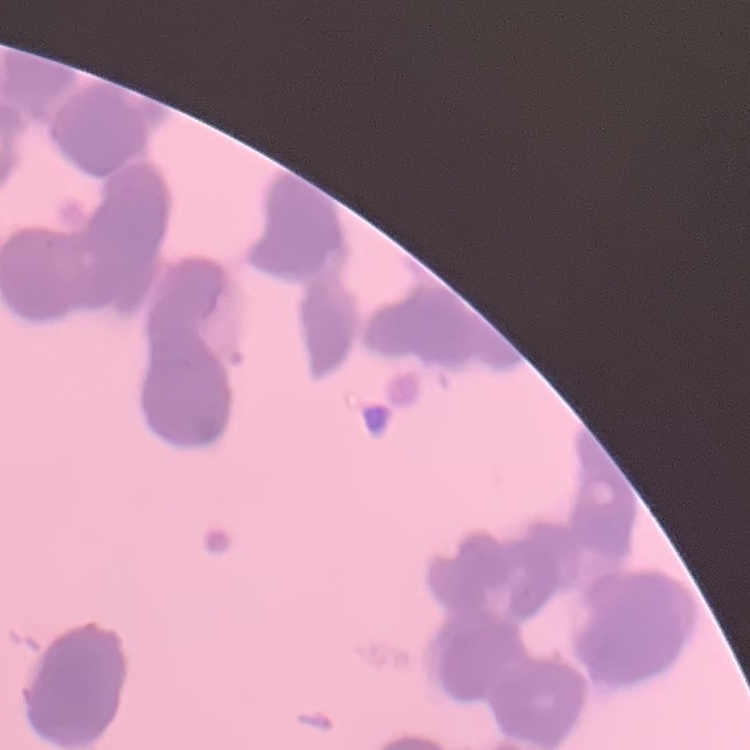
red_blood_cell_morphology: rouleaux formation
preparation: thin blood film
image_type: one tile cut from a larger photomicrograph
stain: Field's or Giemsa